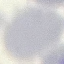

{
  "malaria_status": "uninfected",
  "stain": "Giemsa",
  "capture": "smartphone camera at the microscope eyepiece",
  "image_type": "automatically extracted cell patch, resized to 64 × 64 pixels",
  "preparation": "thin blood smear"
}